Assess the morphology of the erythrocytes.
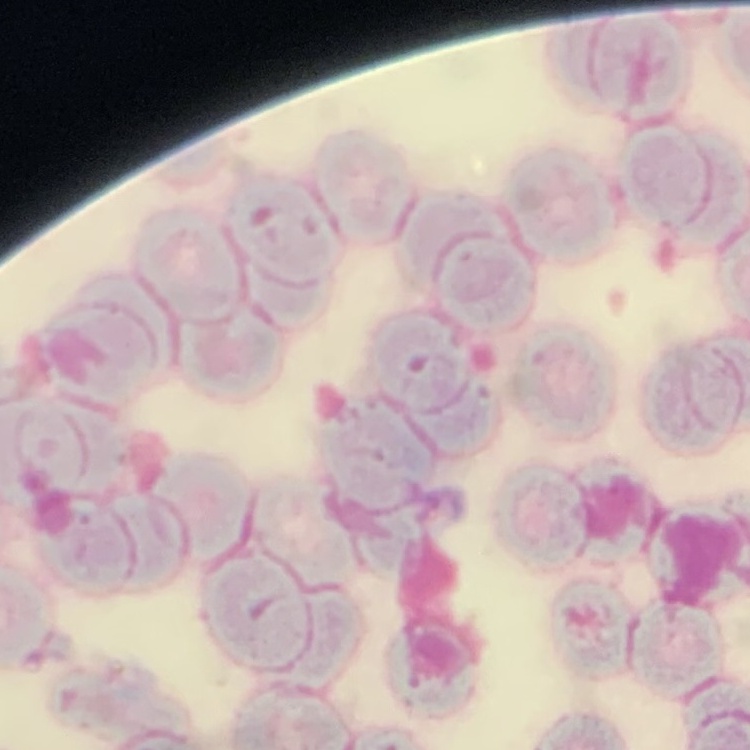

Rouleaux formation.

preparation = thin blood smear
stain = Field's or Giemsa
image type = square crop of a larger photomicrograph